Classify this cell by malaria status.
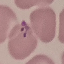
Parasitized.

image type = cell patch, automatically extracted from a larger field of view and resized to 64 × 64 pixels
preparation = thin smear
stain = Giemsa
capture = smartphone camera at the microscope eyepiece